Locate every Babesia divergens-infected red blood cell.
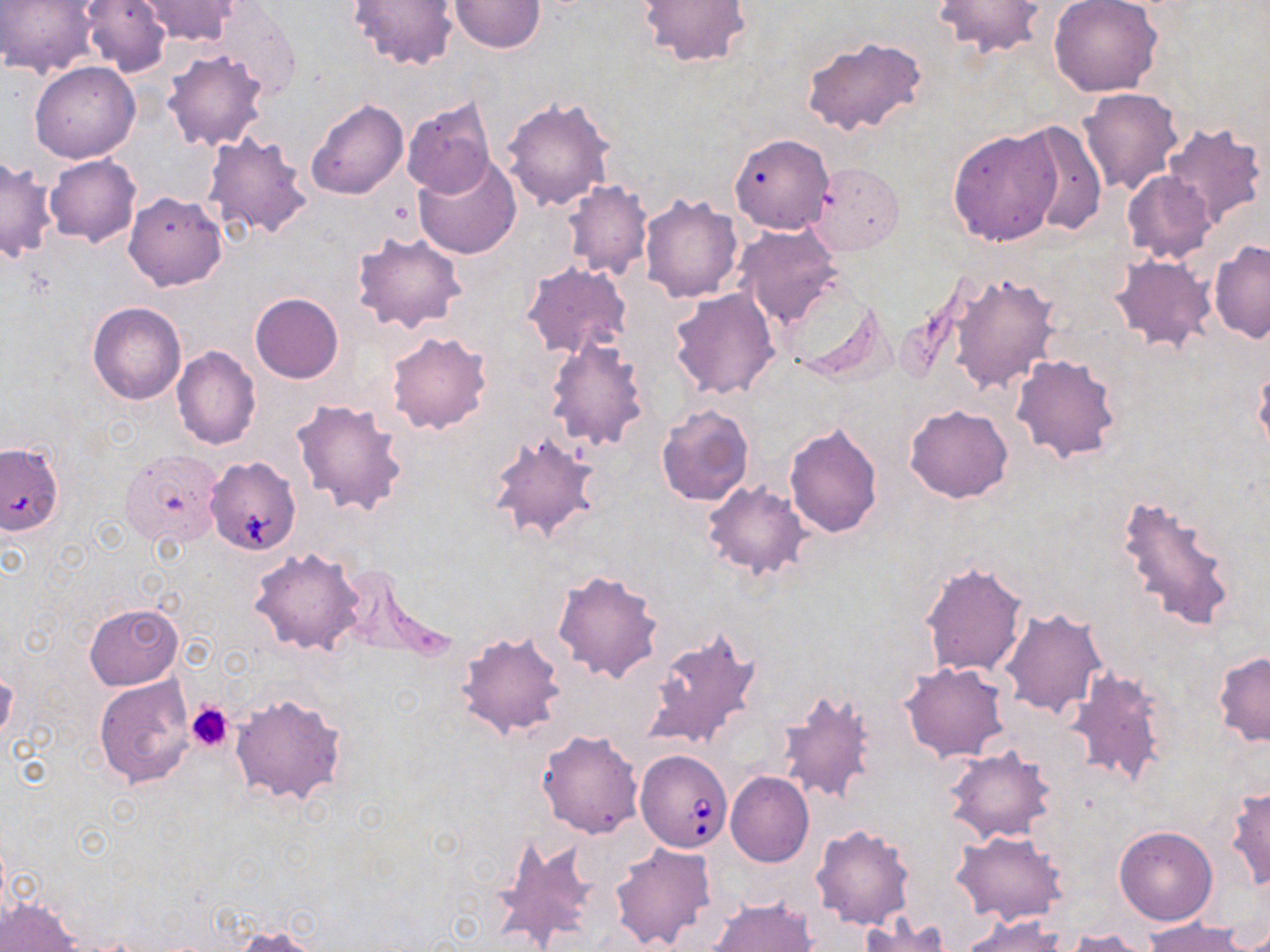

Approximate bounding boxes as (x1,y1)-(x2,y2) corner pairs in pixels.
Babesia divergens-infected red blood cells: (207,458)-(300,554), (638,750)-(734,852).

Summary:
  - Platelet locations: (186,703)-(233,751)
  - Uninfected red blood cell locations: (0,0)-(103,77), (79,0)-(172,78), (349,0)-(460,70), (450,0)-(545,53), (638,0)-(753,69), (931,0)-(1045,58), (1048,0)-(1163,98), (138,1)-(242,44), (201,3)-(302,99), (800,36)-(928,138), (161,49)-(270,151), (29,61)-(140,163), (1078,87)-(1185,196), (402,95)-(497,200), (501,95)-(616,211), (307,99)-(408,199), (1013,121)-(1106,237), (1161,121)-(1267,231), (946,127)-(1065,247), (201,131)-(312,241), (729,133)-(835,234), (44,153)-(140,247), (0,155)-(58,262), (414,155)-(522,259), (810,162)-(903,254), (1120,169)-(1217,265), (562,181)-(652,281), (125,192)-(227,291), (640,194)-(743,303), (733,223)-(843,328), (350,231)-(467,333), (1209,240)-(1270,343), (1109,255)-(1216,353), (522,262)-(632,359), (947,271)-(1060,396), (669,287)-(780,400), (250,293)-(344,383), (792,295)-(893,384), (88,302)-(187,405), (385,332)-(492,435), (545,338)-(650,452), (172,346)-(261,450), (1010,354)-(1121,463), (1253,367)-(1270,465), (291,397)-(409,517), (656,403)-(755,506), (905,404)-(1014,503), (784,421)-(883,538), (485,429)-(603,547), (0,442)-(64,536), (120,449)-(224,549), (701,481)-(811,579), (1113,493)-(1238,635), (250,547)-(365,655), (918,560)-(1029,680), (551,568)-(665,685), (84,603)-(183,689), (1000,607)-(1109,718), (641,625)-(762,753), (456,629)-(567,742), (1213,651)-(1270,748), (899,661)-(1009,762), (1063,666)-(1172,791), (0,670)-(18,746), (93,675)-(196,788), (776,686)-(878,807), (231,693)-(345,805), (537,729)-(645,838), (943,745)-(1057,844), (725,771)-(814,867), (1226,785)-(1269,891), (810,823)-(917,930), (1114,825)-(1218,925), (950,829)-(1068,925), (496,837)-(605,951), (609,843)-(716,951), (1,895)-(80,952), (708,896)-(818,952), (857,914)-(951,952), (960,914)-(1067,951), (1142,918)-(1253,951), (229,923)-(327,951), (1062,928)-(1156,951)
  - Slide-level diagnosis: Babesia divergens
  - Field of view: one of a larger specimen
  - Preparation: thin blood film
  - Stain: May-Grünwald-Giemsa
  - Magnification: 1000x
  - Image size: 1270×952 pixels
  - Modality: light microscopy